State which parasite is depicted.
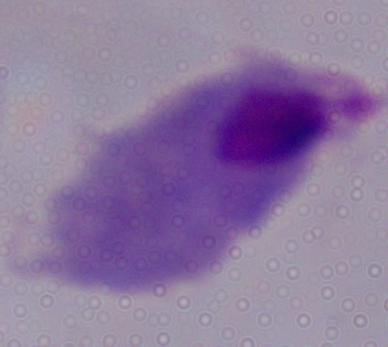

A trichomonad.

modality = photomicrograph
magnification = 1000x